Assess the morphology of the red blood cells.
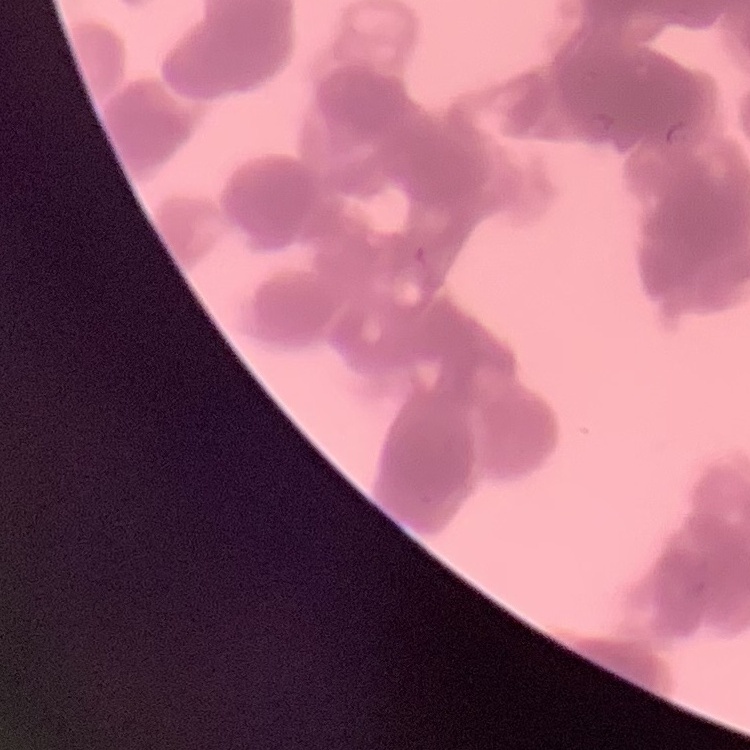
They show rouleaux formation.

image type = one tile cut from a larger photomicrograph
stain = Field's or Giemsa
preparation = thin blood smear